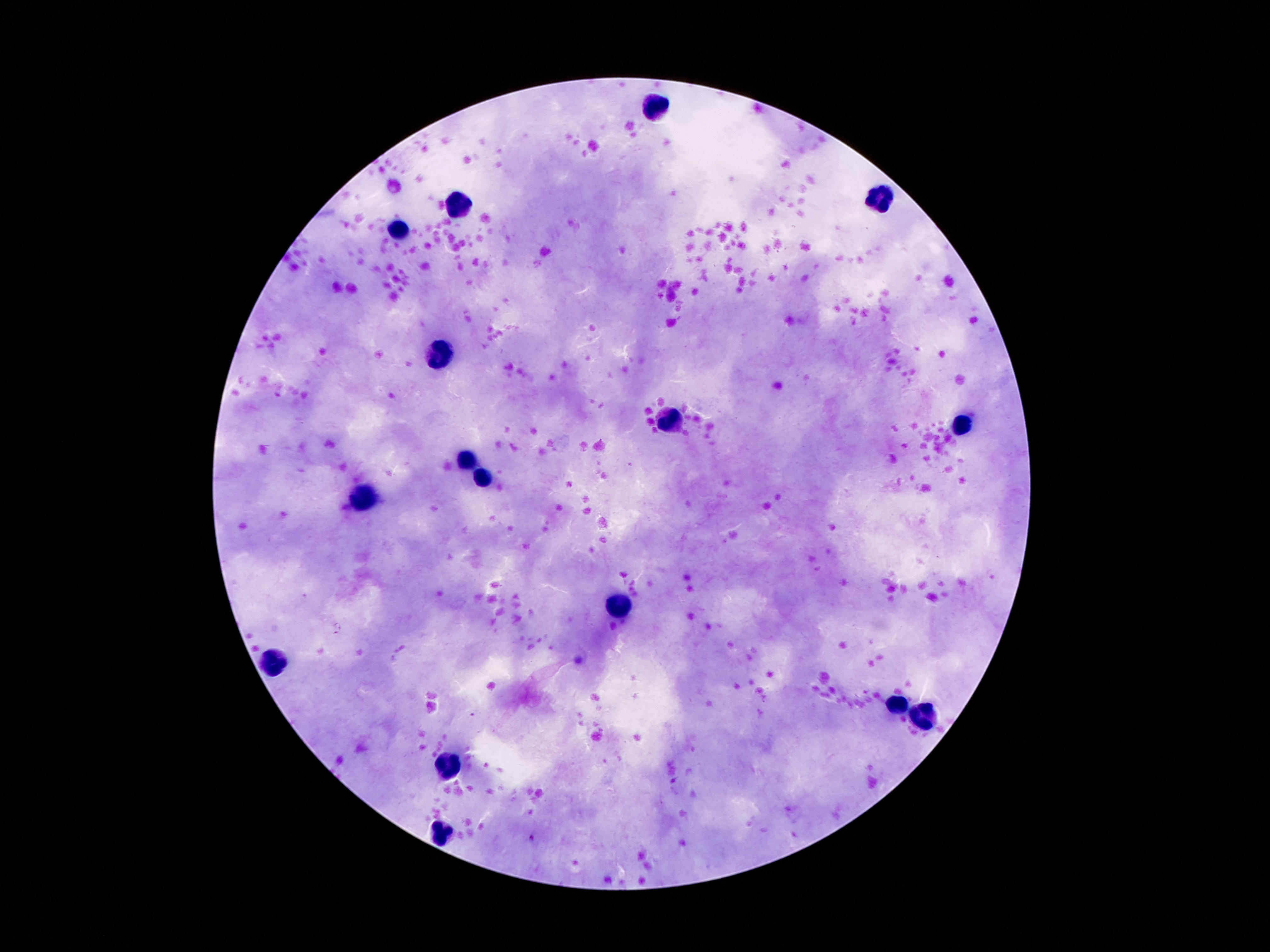

Approximate centers as [x, y] in pixels.
Summary:
  - Leukocyte locations: [652, 108], [877, 197], [457, 204], [398, 230], [438, 356], [667, 419], [963, 423], [463, 459], [484, 473], [361, 498], [619, 605], [281, 663], [898, 706], [923, 719], [451, 765], [444, 833]
  - Stain: Giemsa
  - Capture: smartphone camera through the microscope eyepiece
  - Magnification: 100x
  - Image size: 1270×952 pixels
  - Patient malaria status: not infected
  - Preparation: thick blood smear
  - Field of view: single